Report the malaria status of this cell.
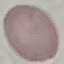
Uninfected.

capture = smartphone through the microscope eyepiece
preparation = thin blood smear
stain = Giemsa
image type = automatically extracted cell patch, resized to 64 × 64 pixels